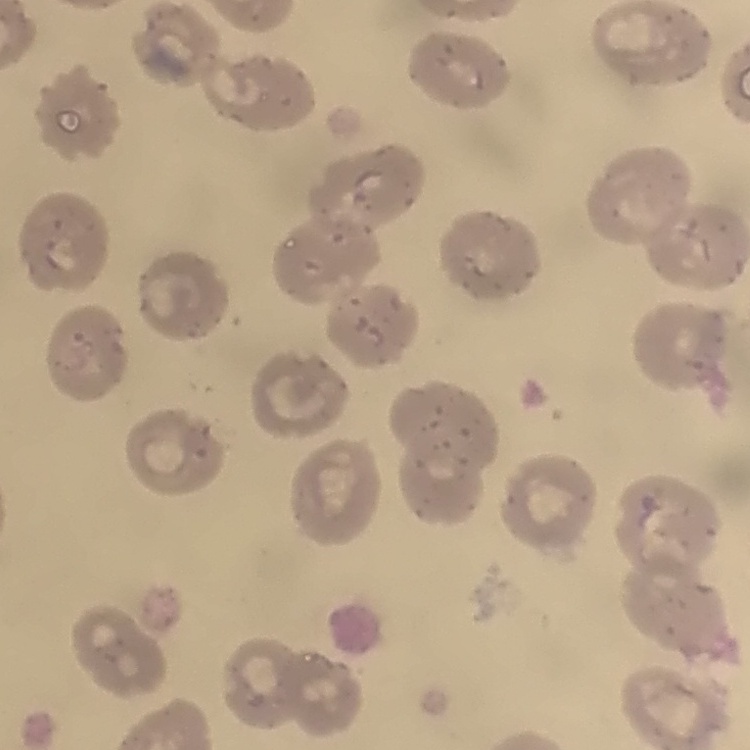 The erythrocytes exhibit no rouleaux formation. Stained with either Field's or Giemsa. Thin blood smear. One tile cut from a larger photomicrograph.